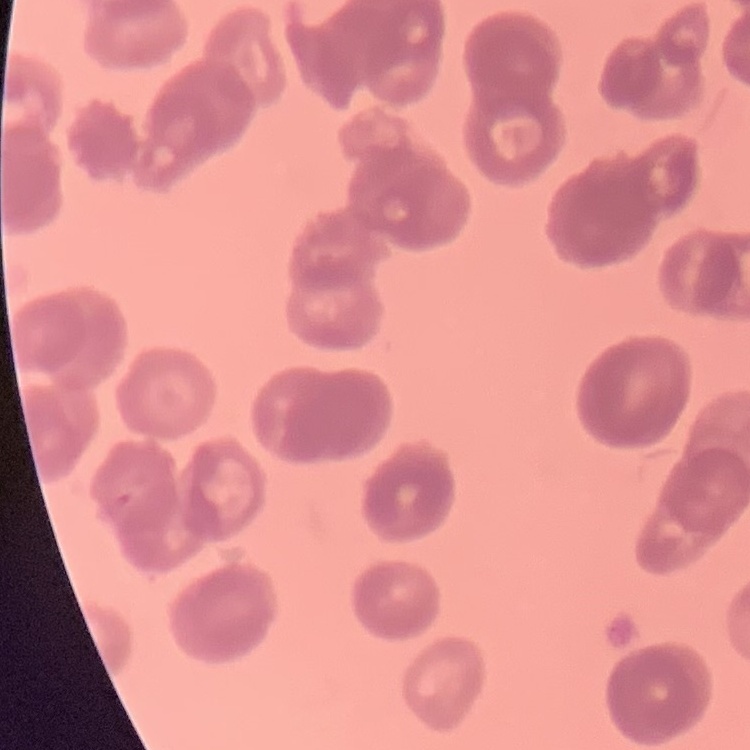
The erythrocytes exhibit rouleaux formation. One tile cut from a larger photomicrograph. Thin blood smear. Field's or Giemsa stain.